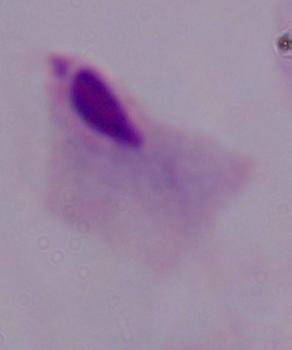

Summary:
  - Magnification: 1000x
  - Identification: trichomonad
  - Modality: photomicrograph